Point out each leukocyte.
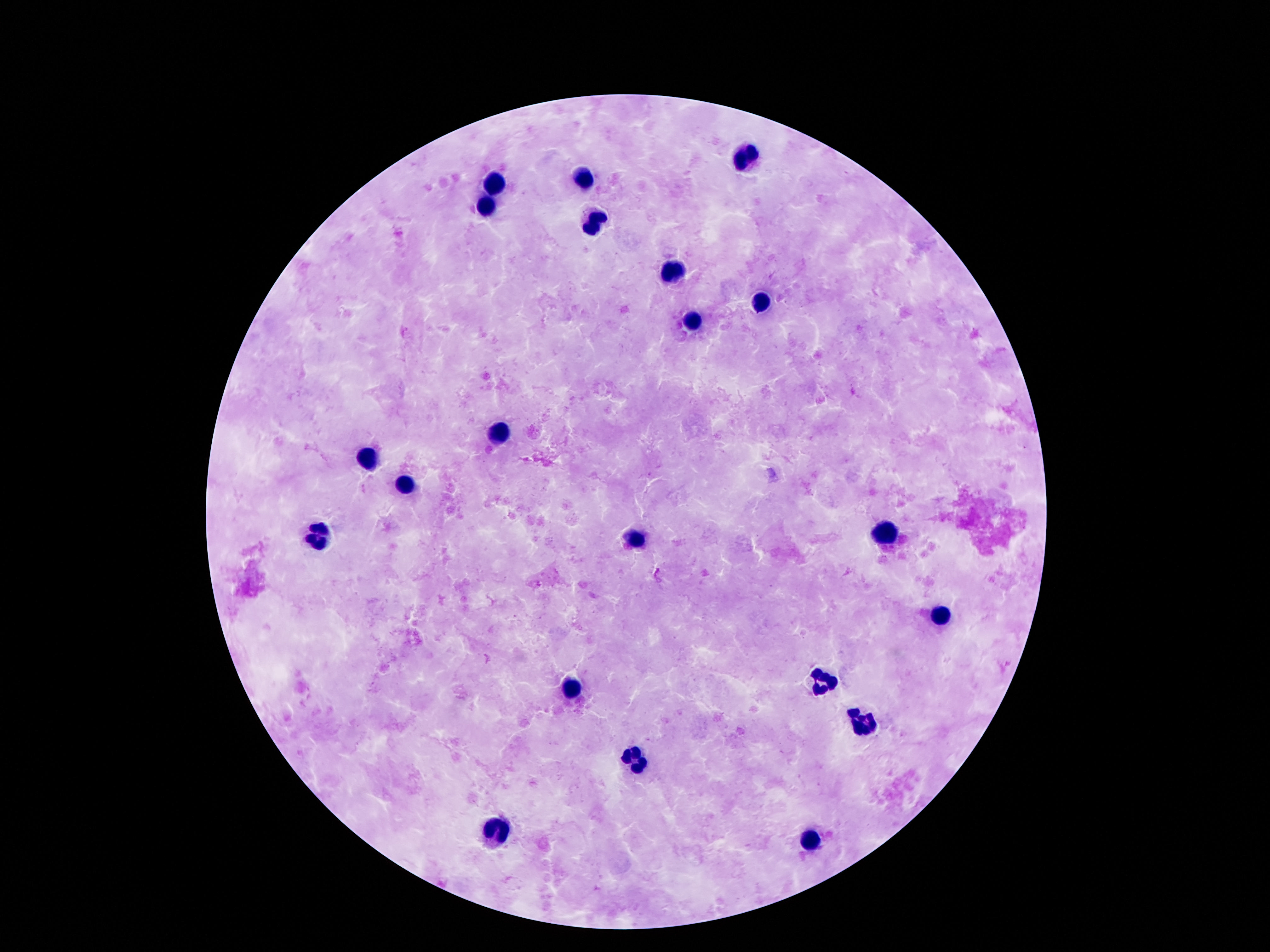
Approximate centers as [x, y] in pixels.
Leukocytes: [749, 157], [582, 179], [493, 181], [487, 202], [586, 221], [672, 269], [760, 302], [693, 321], [498, 433], [369, 461], [407, 491], [319, 536], [886, 536], [636, 538], [940, 612], [825, 675], [573, 690], [863, 719], [632, 758], [498, 832], [812, 841].

image size = 1270×952 pixels
capture = smartphone camera through the microscope eyepiece
magnification = 100x
preparation = thick blood film
patient malaria status = not infected
stain = Giemsa
field of view = one from this slide